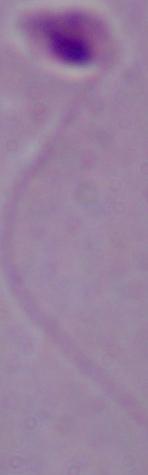

identification = Leishmania
magnification = 1000x
modality = photomicrograph